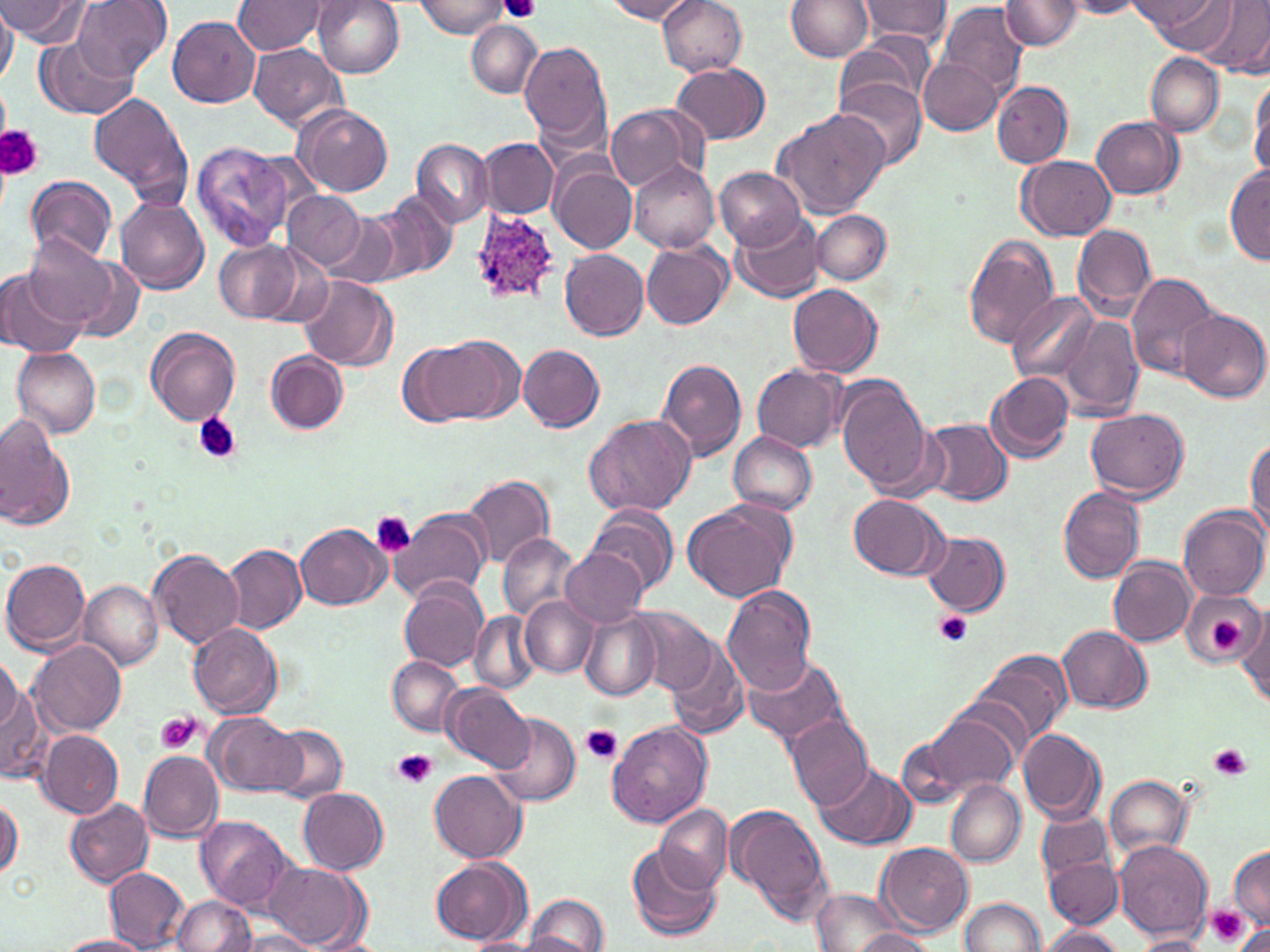 Approximate bounding boxes as (x1, y1, x2, y2) in pixels. Plasmodium ovale-infected red blood cell locations: (468, 209, 561, 306). Platelet locations: (504, 0, 538, 22), (0, 125, 41, 179), (193, 412, 241, 463), (372, 512, 416, 556), (934, 610, 974, 648), (1210, 619, 1242, 651), (157, 712, 201, 754), (579, 723, 622, 764), (1210, 744, 1252, 780), (392, 749, 436, 789), (1207, 905, 1250, 948). Uninfected red blood cell locations: (5, 0, 92, 46), (75, 0, 169, 79), (311, 0, 404, 78), (602, 0, 701, 23), (656, 0, 749, 76), (856, 0, 952, 44), (938, 0, 1028, 98), (1000, 0, 1082, 50), (1057, 0, 1144, 19), (1136, 0, 1233, 51), (1197, 0, 1270, 73), (234, 1, 329, 56), (413, 1, 509, 38), (785, 1, 874, 62), (0, 7, 18, 86), (166, 13, 261, 108), (467, 20, 541, 98), (40, 36, 137, 119), (835, 36, 934, 115), (520, 41, 611, 146), (248, 43, 346, 130), (1146, 52, 1224, 135), (919, 58, 1004, 135), (673, 62, 771, 145), (1249, 75, 1270, 180), (834, 77, 928, 173), (991, 82, 1074, 167), (89, 92, 191, 205), (607, 104, 701, 191), (293, 105, 392, 196), (774, 107, 893, 219), (1092, 115, 1184, 199), (411, 138, 492, 226), (480, 139, 559, 219), (192, 142, 295, 252), (1017, 154, 1117, 241), (630, 161, 720, 254), (551, 165, 637, 255), (1227, 165, 1270, 265), (716, 167, 805, 250), (25, 175, 117, 265), (371, 189, 457, 284), (285, 190, 366, 269), (116, 198, 210, 294), (321, 210, 402, 289), (812, 210, 891, 285), (732, 212, 825, 303), (1073, 223, 1156, 316), (23, 235, 118, 328), (962, 235, 1061, 347), (213, 239, 303, 323), (641, 240, 734, 330), (62, 249, 147, 343), (560, 249, 649, 340), (1, 271, 85, 358), (1125, 272, 1220, 379), (298, 277, 397, 371), (788, 282, 882, 377), (1009, 290, 1100, 384), (1174, 308, 1267, 403), (1057, 314, 1145, 421), (145, 327, 241, 426), (419, 336, 522, 425), (518, 344, 605, 432), (13, 347, 102, 438), (266, 351, 348, 433), (655, 358, 748, 463), (752, 364, 846, 452), (984, 371, 1074, 463), (835, 376, 932, 494), (1087, 408, 1190, 500), (585, 414, 698, 518), (0, 417, 74, 530), (922, 417, 1012, 506), (727, 431, 818, 515), (1246, 436, 1270, 538), (462, 473, 555, 568), (1058, 486, 1146, 583), (847, 493, 947, 579), (682, 498, 796, 602), (586, 504, 678, 597), (1178, 504, 1269, 601), (388, 507, 492, 604), (296, 523, 388, 610), (922, 530, 1010, 616), (498, 533, 577, 622), (222, 544, 306, 635), (150, 548, 244, 648), (563, 549, 647, 629), (1108, 557, 1196, 647), (2, 558, 91, 654), (77, 579, 165, 670), (397, 579, 488, 672), (721, 584, 817, 694), (1182, 590, 1265, 669), (521, 597, 598, 677), (625, 605, 718, 695), (577, 609, 659, 701), (469, 612, 538, 696), (1236, 613, 1268, 708), (187, 622, 283, 720), (1058, 627, 1152, 714), (27, 640, 126, 736), (666, 640, 751, 741), (973, 648, 1073, 747), (743, 653, 850, 747), (0, 654, 24, 738), (388, 655, 464, 736), (0, 669, 42, 784), (442, 682, 534, 772), (917, 704, 1024, 797), (204, 711, 305, 797), (489, 711, 582, 808), (786, 714, 875, 811), (607, 719, 711, 827), (271, 724, 348, 802), (895, 726, 980, 813), (1018, 728, 1106, 823), (39, 729, 123, 818), (138, 749, 225, 843), (814, 760, 915, 849), (429, 769, 527, 863), (1104, 775, 1192, 860), (946, 778, 1026, 866), (299, 788, 389, 875), (1, 796, 23, 881), (65, 799, 153, 886), (724, 803, 832, 924), (656, 804, 733, 891), (1037, 811, 1113, 880), (196, 815, 297, 912), (1114, 839, 1212, 941), (878, 841, 974, 934), (626, 844, 723, 940), (1229, 847, 1270, 931), (430, 855, 533, 946), (1046, 858, 1122, 928), (264, 862, 370, 950), (105, 868, 189, 951), (812, 888, 907, 952), (525, 894, 610, 951), (171, 895, 256, 952), (959, 897, 1044, 952), (1038, 926, 1126, 952), (850, 928, 937, 951), (234, 930, 324, 951), (1134, 932, 1213, 950), (309, 933, 385, 952), (58, 935, 153, 952), (464, 937, 538, 952). Slide-level diagnosis: Plasmodium ovale. Image is 1270×952 pixels. May-Grünwald-Giemsa-stained preparation. Light microscopy. Thin blood smear. 1000x magnification. One field of a larger specimen.